Locate and identify every blood parasite.
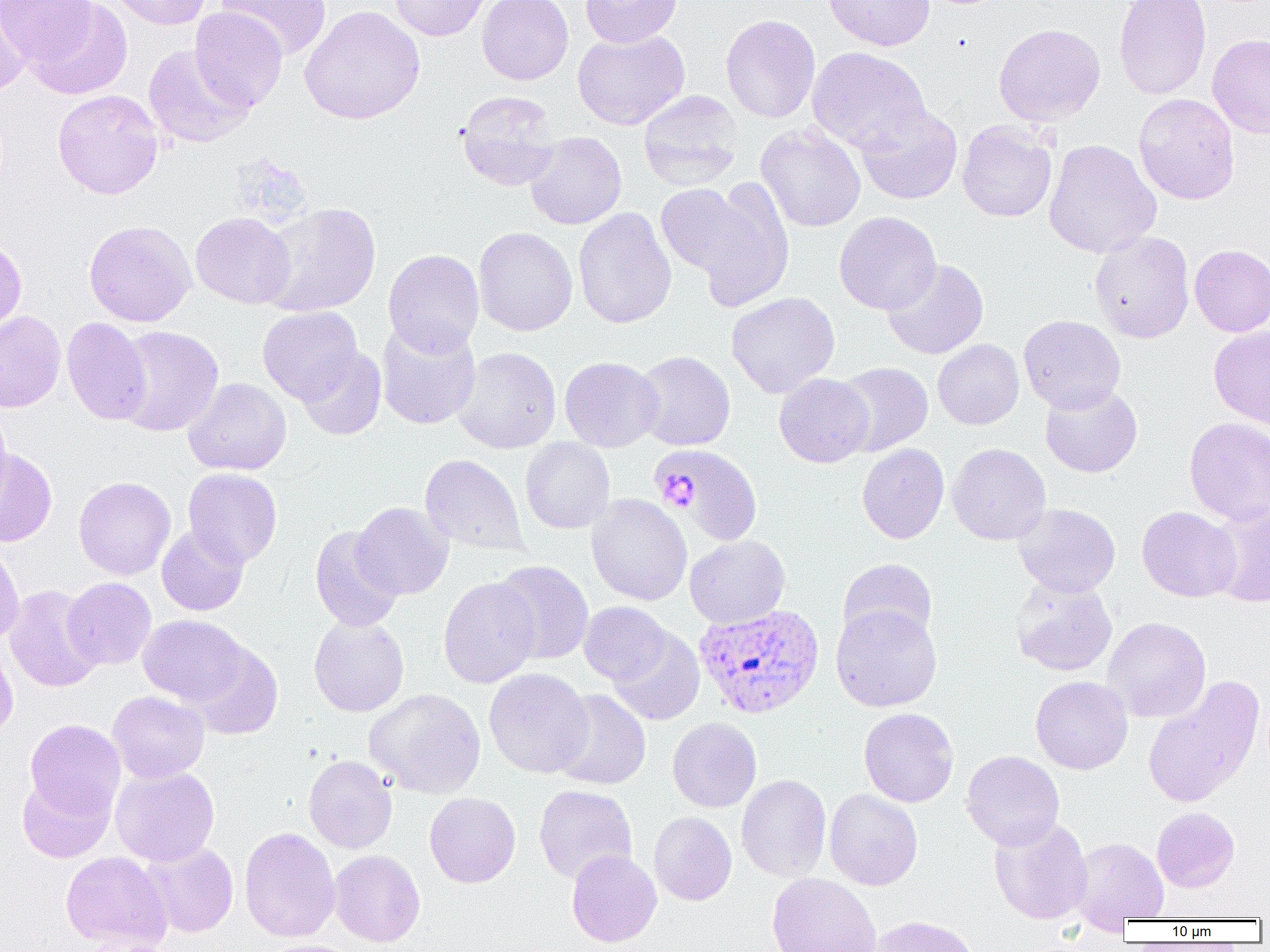

Approximate bounding boxes as (x1,y1)-(x2,y2) corner pairs in pixels.
Plasmodium vivax-infected red blood cells: (694,603)-(825,719).
No Plasmodium falciparum, Plasmodium ovale, Plasmodium malariae, Babesia divergens, or Trypanosoma brucei observed.

{
  "slide_level_diagnosis": "Plasmodium vivax",
  "modality": "light microscopy",
  "preparation": "thin blood smear",
  "uninfected_red_blood_cell_locations": "approximate bounding boxes as (x1,y1)-(x2,y2) corner pairs in pixels: (108,0)-(211,30), (216,0)-(332,61), (388,0)-(493,41), (476,0)-(573,85), (580,0)-(683,47), (823,0)-(935,51), (1113,0)-(1212,100), (0,1)-(97,68), (24,1)-(133,100), (0,2)-(30,94), (299,5)-(425,125), (190,6)-(287,113), (720,14)-(821,124), (993,23)-(1106,126), (572,30)-(690,130), (1207,33)-(1270,139), (143,44)-(254,148), (806,46)-(931,154), (52,89)-(164,200), (456,91)-(561,191), (638,91)-(743,191), (1133,93)-(1240,205), (856,103)-(963,204), (957,120)-(1058,222), (756,124)-(866,232), (524,131)-(626,230), (1043,139)-(1162,258), (693,178)-(793,311), (655,183)-(755,277), (258,202)-(381,316), (573,207)-(677,329), (834,211)-(941,315), (190,212)-(296,309), (84,220)-(196,326), (473,226)-(578,336), (1089,231)-(1195,343), (0,237)-(27,335), (1189,244)-(1270,337), (383,249)-(484,356), (882,258)-(989,359), (726,292)-(840,398), (257,306)-(363,404), (0,311)-(66,412), (1019,315)-(1126,413), (62,317)-(151,425), (376,319)-(481,430), (1209,325)-(1270,430), (113,326)-(224,437), (933,339)-(1024,429), (295,346)-(386,440), (452,346)-(561,454), (633,350)-(736,451), (560,357)-(663,452), (834,361)-(933,456), (774,373)-(873,467), (184,378)-(291,475), (1040,383)-(1143,478), (0,406)-(12,508), (1184,416)-(1270,527), (520,438)-(615,533), (857,443)-(949,544), (947,443)-(1051,545), (646,447)-(766,551), (0,449)-(57,547), (420,454)-(527,556), (183,468)-(283,567), (73,476)-(175,580), (586,494)-(692,606), (352,502)-(453,599), (1013,503)-(1121,597), (1207,503)-(1270,608), (1137,506)-(1241,602), (157,525)-(249,616), (309,525)-(405,632), (685,534)-(790,628), (0,540)-(25,645), (837,558)-(937,648), (492,560)-(593,665), (438,576)-(540,689), (62,577)-(157,670), (1009,578)-(1117,676), (4,584)-(104,693), (579,601)-(672,685), (831,605)-(942,712), (138,615)-(248,706), (309,615)-(409,717), (1103,616)-(1211,723), (607,627)-(704,726), (0,639)-(18,745), (186,641)-(283,740), (484,668)-(594,778), (1030,675)-(1133,775), (1142,675)-(1265,808), (365,688)-(486,798), (551,689)-(651,790), (108,691)-(209,783), (859,707)-(959,807), (667,718)-(762,813), (24,719)-(125,820), (961,750)-(1064,850), (303,755)-(397,853), (110,766)-(220,866), (17,773)-(116,864), (736,774)-(831,883), (534,784)-(637,885), (824,789)-(923,890), (424,792)-(520,887), (1151,807)-(1240,893), (649,812)-(737,906), (989,816)-(1093,925), (239,827)-(340,942), (1070,837)-(1168,924), (140,841)-(239,938), (61,850)-(171,950), (329,850)-(425,947), (566,850)-(661,947), (766,873)-(882,952), (867,914)-(981,952), (81,938)-(181,952), (261,939)-(362,952)",
  "field_of_view": "one of a larger specimen",
  "platelet_locations": "approximate bounding boxes as (x1,y1)-(x2,y2) corner pairs in pixels: (654,474)-(700,512)",
  "image_size": "1270×952 pixels",
  "magnification": "1000x"
}